Outline each blood parasite and name the species.
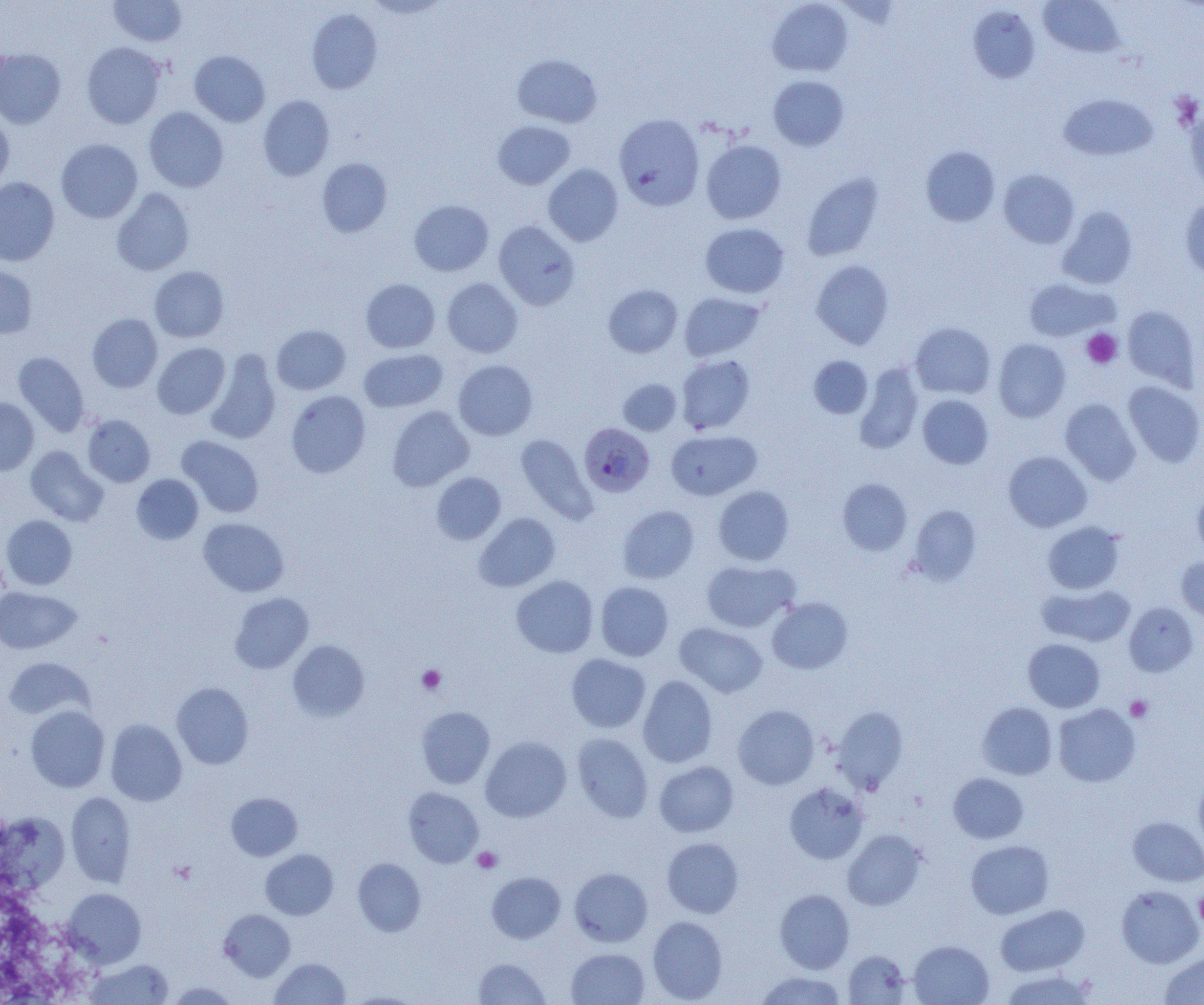
Approximate bounding boxes as (x1, y1, x2, y2) in pixels.
Plasmodium falciparum-infected red blood cells: (579, 423, 655, 497).
No Plasmodium ovale, Plasmodium malariae, Plasmodium vivax, Babesia divergens, or Trypanosoma brucei observed.

{
  "slide_level_diagnosis": "Plasmodium falciparum",
  "field_of_view": "single",
  "modality": "light microscopy",
  "magnification": "1000x",
  "image_size": "1204×1005 pixels",
  "preparation": "thin blood film",
  "platelet_locations": "approximate bounding boxes as (x1, y1, x2, y2) in pixels: (1082, 328, 1122, 368), (417, 665, 446, 694), (1125, 695, 1152, 722), (472, 847, 502, 873), (169, 860, 197, 885), (1194, 890, 1204, 930)",
  "uninfected_red_blood_cell_locations": "approximate bounding boxes as (x1, y1, x2, y2) in pixels: (109, 0, 187, 46), (1039, 0, 1126, 58), (767, 1, 853, 77), (968, 5, 1040, 84), (306, 8, 383, 94), (81, 42, 167, 128), (0, 48, 66, 128), (189, 50, 270, 126), (512, 54, 602, 127), (768, 75, 849, 151), (1058, 93, 1158, 161), (258, 95, 335, 181), (1184, 105, 1204, 196), (144, 107, 229, 192), (613, 113, 705, 210), (0, 114, 14, 191), (493, 120, 575, 190), (56, 138, 143, 223), (701, 139, 787, 224), (920, 146, 1000, 226), (316, 158, 392, 237), (543, 163, 624, 247), (998, 169, 1080, 249), (802, 173, 884, 261), (0, 177, 59, 266), (111, 187, 194, 276), (1180, 198, 1204, 279), (409, 200, 494, 277), (1056, 207, 1137, 289), (493, 220, 580, 310), (700, 223, 789, 298), (810, 259, 895, 349), (0, 264, 37, 339), (149, 266, 229, 343), (1022, 277, 1117, 342), (360, 278, 440, 353), (442, 278, 523, 358), (603, 284, 683, 357), (679, 292, 764, 362), (1122, 305, 1200, 390), (86, 313, 163, 392), (910, 322, 996, 399), (271, 324, 351, 395), (993, 339, 1071, 422), (152, 342, 230, 418), (358, 348, 448, 412), (205, 350, 281, 445), (13, 351, 90, 437), (676, 354, 755, 434), (808, 356, 873, 418), (453, 360, 538, 440), (854, 363, 924, 454), (618, 378, 682, 435), (1123, 381, 1204, 467), (286, 390, 370, 478), (918, 394, 994, 469), (0, 397, 39, 475), (1060, 398, 1141, 485), (387, 406, 474, 491), (82, 414, 155, 487), (665, 430, 761, 500), (515, 434, 597, 524), (177, 435, 264, 518), (25, 446, 108, 526), (1003, 451, 1092, 532), (431, 472, 506, 545), (131, 474, 203, 545), (837, 478, 912, 555), (712, 485, 794, 565), (1192, 488, 1204, 560), (618, 505, 699, 584), (908, 505, 982, 585), (473, 513, 560, 592), (2, 515, 77, 590), (198, 517, 289, 597), (1042, 521, 1125, 594), (1176, 557, 1204, 621), (701, 559, 799, 632), (511, 575, 598, 658), (595, 581, 674, 661), (1037, 583, 1135, 647), (0, 587, 81, 654), (229, 592, 314, 673), (768, 597, 853, 674), (1124, 602, 1199, 676), (675, 623, 767, 697), (1023, 638, 1105, 712), (288, 640, 369, 722), (566, 653, 650, 733), (3, 657, 94, 722), (637, 676, 718, 767), (172, 682, 254, 769), (977, 702, 1057, 780), (1053, 703, 1140, 787), (733, 704, 819, 789), (25, 706, 109, 792), (416, 706, 495, 788), (831, 706, 909, 794), (106, 719, 187, 806), (573, 733, 653, 822), (480, 736, 571, 822), (654, 761, 739, 837), (1193, 772, 1204, 856), (949, 773, 1028, 843), (784, 782, 868, 864), (403, 787, 483, 867), (66, 792, 136, 887), (226, 792, 302, 861), (1, 813, 69, 893), (1128, 817, 1204, 887), (842, 829, 926, 910), (662, 837, 744, 918), (965, 840, 1054, 919), (260, 849, 338, 920), (353, 858, 426, 936), (569, 867, 652, 946), (486, 872, 565, 943), (1116, 885, 1203, 968), (62, 888, 146, 968), (774, 889, 855, 973), (995, 904, 1090, 976), (219, 909, 295, 981), (647, 916, 728, 1003), (908, 940, 994, 1005), (566, 948, 649, 1005), (843, 950, 911, 1004), (1159, 952, 1204, 1004), (85, 958, 174, 1004), (270, 958, 350, 1004), (474, 958, 550, 1004), (998, 969, 1098, 1005), (754, 970, 848, 1005), (167, 981, 239, 1004), (343, 992, 423, 1005)"
}